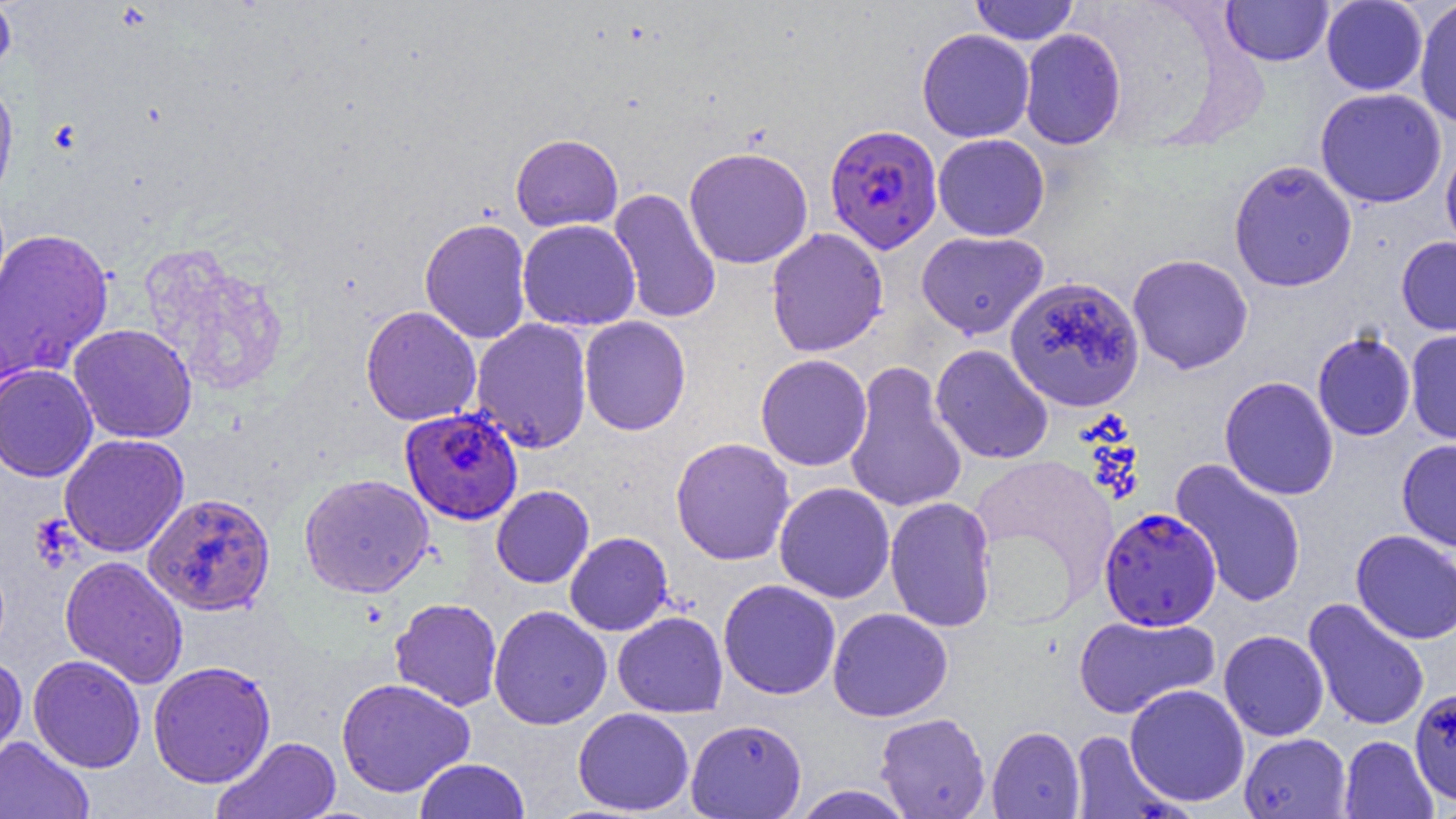
Summary:
  - Coordinate format: approximate bounding boxes as (x1,y1)-(x2,y2) corner pairs in pixels
  - Uninfected red blood cell locations: (0,0)-(16,78), (970,0)-(1079,45), (1222,0)-(1334,66), (1321,1)-(1428,95), (1414,1)-(1456,128), (917,28)-(1035,143), (1019,28)-(1126,150), (0,79)-(19,206), (1315,88)-(1447,208), (510,133)-(623,232), (933,133)-(1050,241), (1441,143)-(1456,259), (683,146)-(814,269), (1229,159)-(1358,292), (608,188)-(722,324), (419,217)-(532,344), (517,219)-(641,331), (0,227)-(114,382), (766,227)-(888,357), (916,231)-(1048,339), (1397,237)-(1456,336), (140,245)-(288,397), (1127,254)-(1254,374), (1005,276)-(1145,412), (360,305)-(481,426), (578,316)-(691,436), (471,318)-(593,453), (68,323)-(197,443), (1405,329)-(1456,445), (1312,331)-(1416,441), (931,344)-(1053,464), (755,353)-(872,471), (844,361)-(968,515), (0,364)-(98,482), (1219,376)-(1339,500), (58,434)-(189,557), (670,437)-(795,565), (1397,439)-(1456,551), (968,454)-(1118,612), (1170,458)-(1308,608), (299,473)-(434,598), (774,482)-(895,603), (491,485)-(594,588), (136,490)-(269,614), (884,496)-(997,632), (1351,530)-(1456,644), (564,532)-(673,636), (60,555)-(188,689), (718,579)-(841,699), (390,598)-(503,711), (1303,598)-(1430,731), (488,605)-(612,729), (828,607)-(953,722), (613,611)-(728,718), (1073,614)-(1220,719), (1218,630)-(1329,741), (0,655)-(28,768), (27,655)-(146,773), (148,660)-(276,787), (336,677)-(475,797), (1125,683)-(1250,807), (1410,692)-(1456,809), (573,708)-(694,815), (875,712)-(991,818), (686,718)-(807,818), (987,726)-(1084,819), (1069,730)-(1182,818), (1239,732)-(1352,818), (0,736)-(93,819), (212,736)-(341,819), (1339,736)-(1437,818), (414,758)-(529,819), (790,784)-(916,819)
  - Plasmodium falciparum-infected red blood cell locations: (824,123)-(943,254), (400,407)-(523,525), (1099,508)-(1221,630)
  - Slide-level diagnosis: Plasmodium falciparum
  - Field of view: single
  - Preparation: thin blood film
  - Magnification: 1000x
  - Modality: optical microscopy
  - Image size: 1456×819 pixels